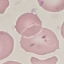
{
  "result": "negative for malaria parasites",
  "stain": "Giemsa",
  "image_type": "automatically extracted cell patch, resized to 64 × 64 pixels",
  "capture": "smartphone through the microscope eyepiece",
  "preparation": "thin smear"
}